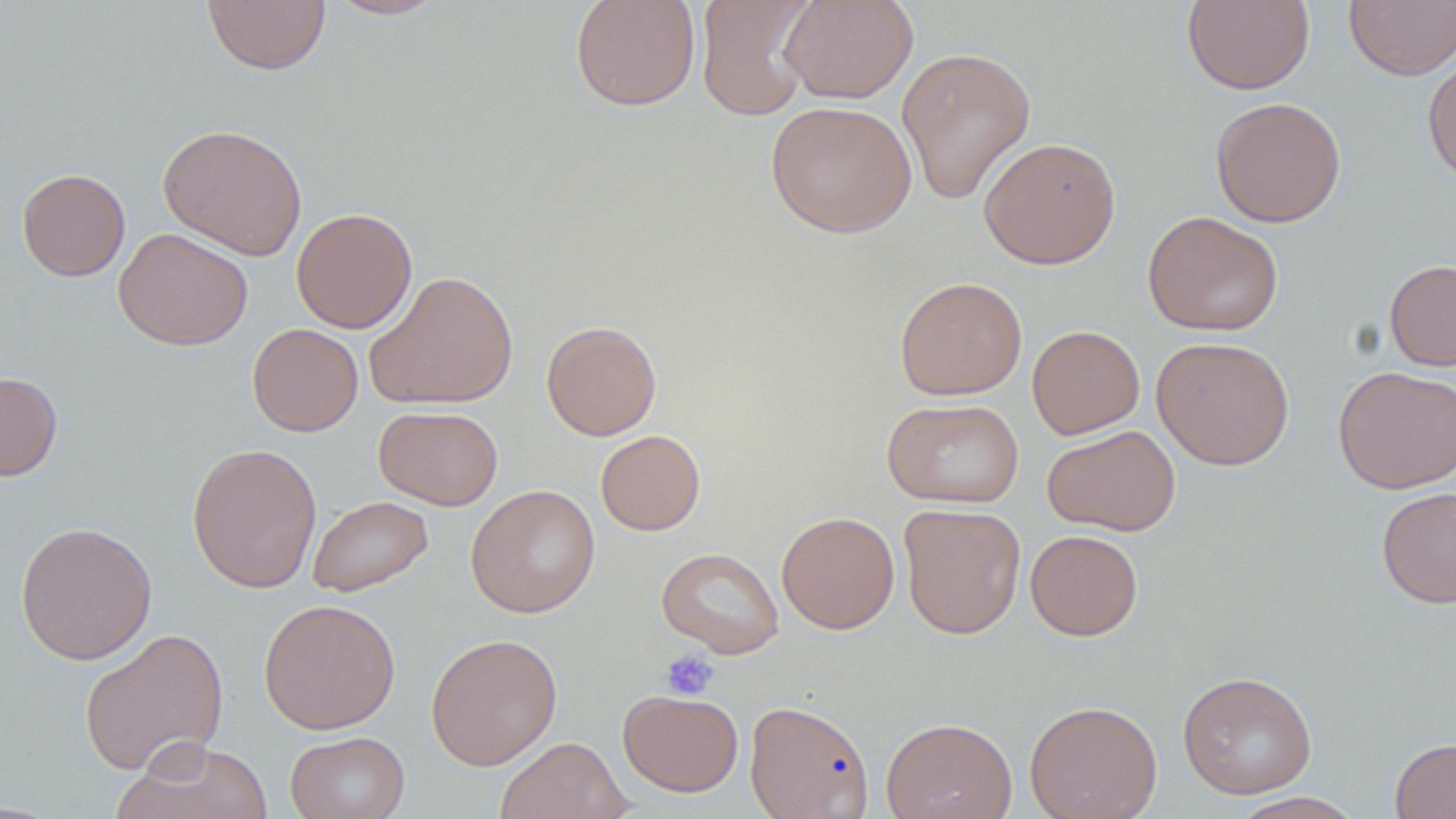 Approximate bounding boxes as named x1/y1/x2/y2 corners in pixels. Uninfected red blood cell locations: (x1=323, y1=0, x2=451, y2=20), (x1=570, y1=0, x2=701, y2=112), (x1=695, y1=0, x2=818, y2=121), (x1=779, y1=0, x2=918, y2=104), (x1=1344, y1=0, x2=1456, y2=80), (x1=202, y1=1, x2=331, y2=75), (x1=1181, y1=1, x2=1315, y2=95), (x1=896, y1=45, x2=1036, y2=205), (x1=1422, y1=52, x2=1456, y2=186), (x1=1210, y1=96, x2=1347, y2=227), (x1=765, y1=100, x2=917, y2=238), (x1=157, y1=123, x2=308, y2=261), (x1=979, y1=136, x2=1121, y2=269), (x1=16, y1=168, x2=130, y2=281), (x1=291, y1=207, x2=418, y2=333), (x1=1142, y1=211, x2=1284, y2=336), (x1=113, y1=227, x2=253, y2=351), (x1=1384, y1=259, x2=1456, y2=372), (x1=363, y1=269, x2=519, y2=411), (x1=894, y1=276, x2=1028, y2=400), (x1=541, y1=320, x2=662, y2=440), (x1=247, y1=323, x2=363, y2=436), (x1=1027, y1=324, x2=1145, y2=439), (x1=1152, y1=336, x2=1295, y2=470), (x1=1332, y1=365, x2=1456, y2=494), (x1=0, y1=371, x2=63, y2=481), (x1=882, y1=397, x2=1024, y2=508), (x1=374, y1=405, x2=503, y2=510), (x1=1042, y1=425, x2=1181, y2=536), (x1=595, y1=430, x2=705, y2=535), (x1=186, y1=441, x2=322, y2=593), (x1=465, y1=484, x2=600, y2=617), (x1=1376, y1=486, x2=1456, y2=609), (x1=307, y1=495, x2=433, y2=598), (x1=898, y1=503, x2=1027, y2=639), (x1=776, y1=511, x2=900, y2=634), (x1=15, y1=521, x2=158, y2=665), (x1=1025, y1=529, x2=1143, y2=641), (x1=656, y1=547, x2=785, y2=658), (x1=258, y1=598, x2=400, y2=734), (x1=78, y1=627, x2=229, y2=776), (x1=425, y1=632, x2=563, y2=770), (x1=1177, y1=670, x2=1317, y2=799), (x1=617, y1=689, x2=744, y2=797), (x1=744, y1=699, x2=874, y2=818), (x1=1024, y1=699, x2=1163, y2=819), (x1=881, y1=716, x2=1018, y2=819), (x1=286, y1=730, x2=409, y2=819), (x1=494, y1=736, x2=632, y2=819), (x1=1390, y1=738, x2=1456, y2=819), (x1=114, y1=739, x2=275, y2=819), (x1=1227, y1=792, x2=1366, y2=819). Platelet locations: (x1=660, y1=649, x2=719, y2=701). Slide-level diagnosis: no evidence of blood parasites. Thin blood smear. Captured at 1000x magnification. Single field of view. Light microscopy. Image is 1456×819 pixels. May-Grünwald-Giemsa stain.